Assess this cell for malaria.
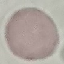
It is uninfected.

Summary:
  - Capture: smartphone through the microscope eyepiece
  - Stain: Giemsa
  - Image type: cell patch, automatically extracted from a larger field of view and resized to 64 × 64 pixels
  - Preparation: thin blood smear